State which parasite is depicted.
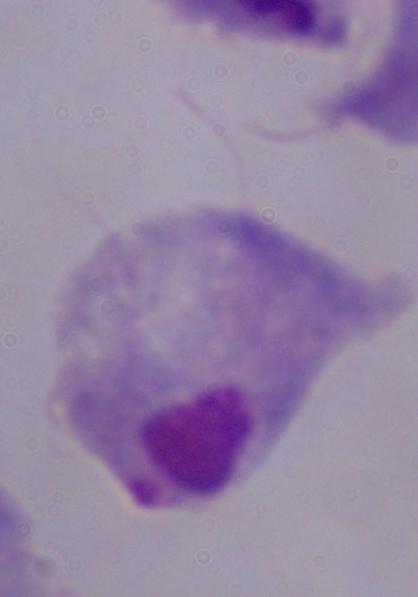
This is a trichomonad.

Photomicrograph. Captured at 1000x magnification.